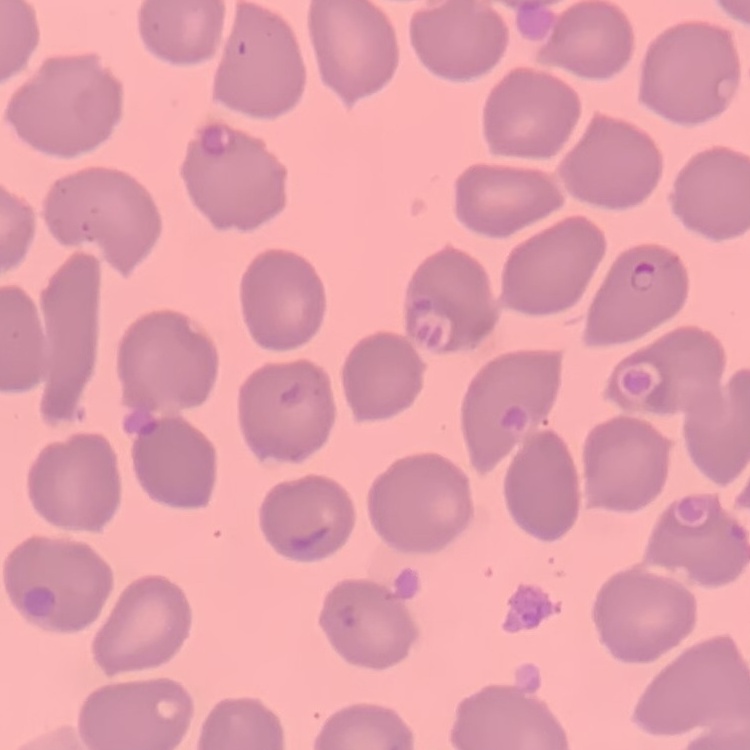

The red blood cells exhibit no rouleaux formation. Square crop of a larger photomicrograph. Stained with either Field's or Giemsa. Thin blood film.